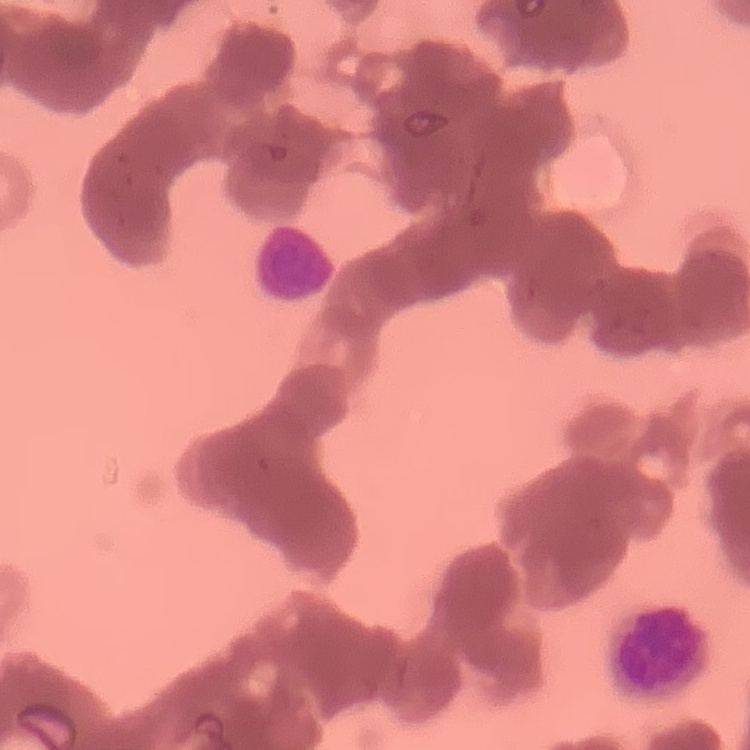

Summary:
  - Red blood cell morphology: rouleaux formation
  - Preparation: thin peripheral smear
  - Image type: one tile cut from a larger photomicrograph
  - Stain: Field's or Giemsa